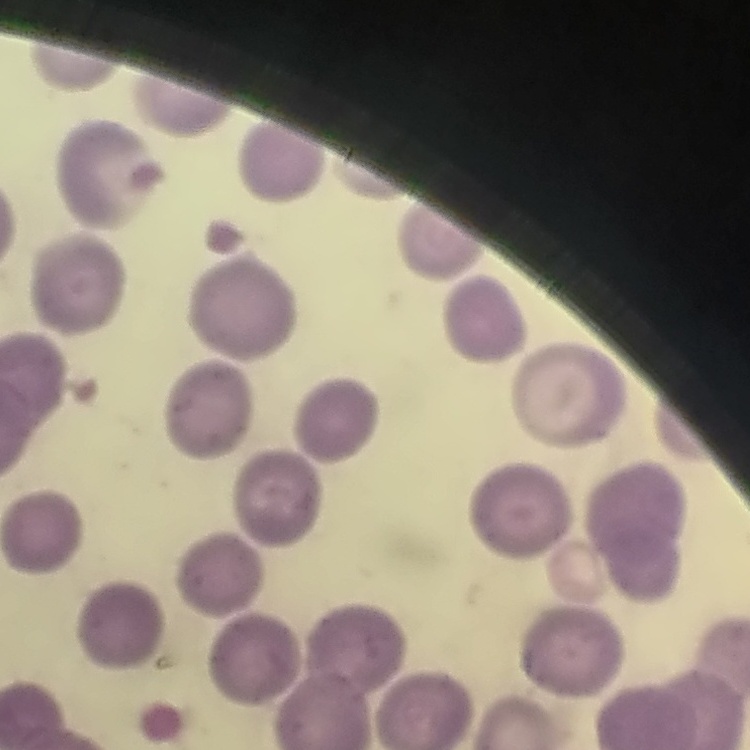

{
  "erythrocyte_morphology": "no rouleaux formation",
  "stain": "Field's or Giemsa",
  "image_type": "one tile cut from a larger photomicrograph",
  "preparation": "thin blood film"
}